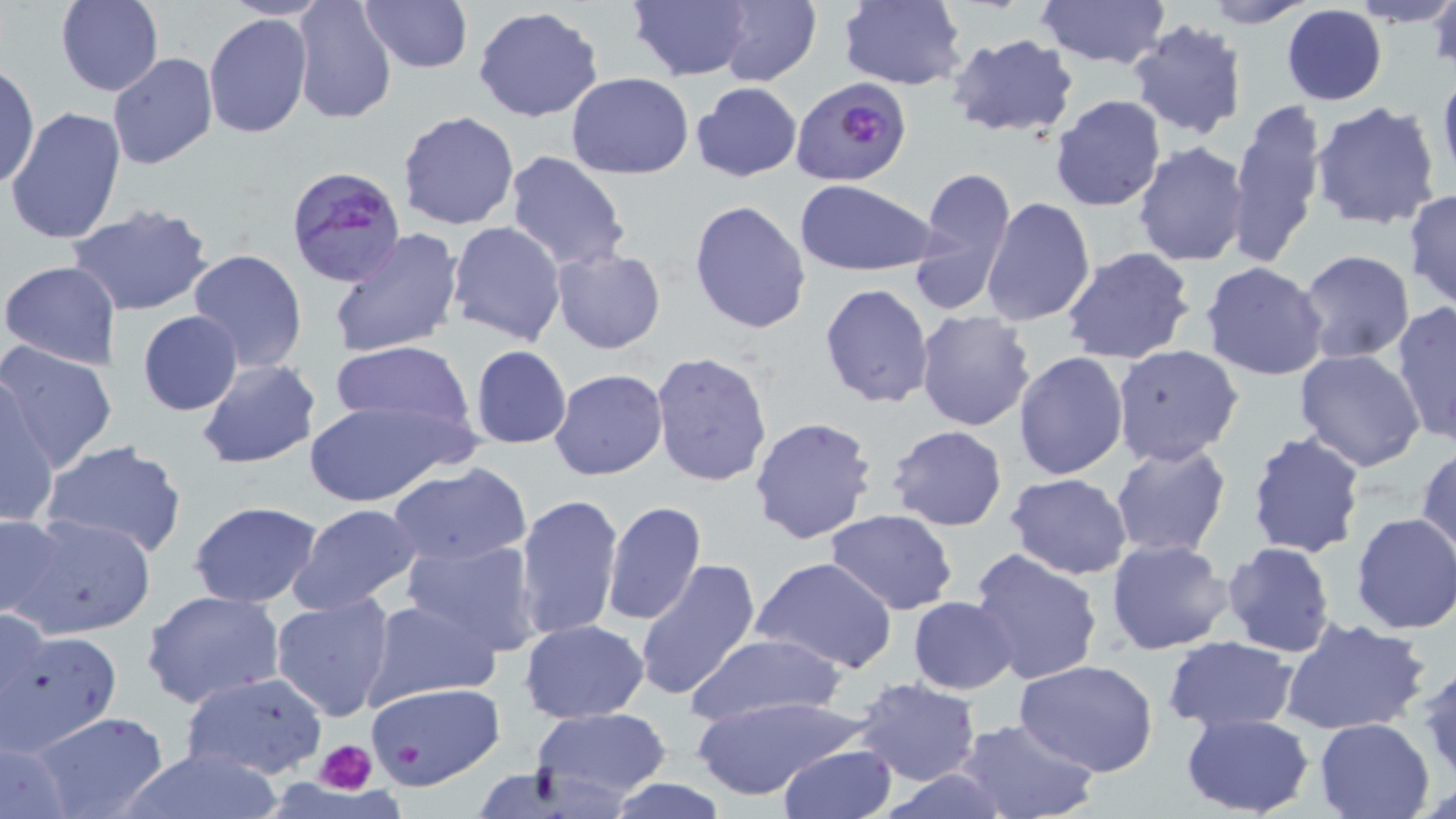 Approximate bounding boxes as (x1,y1)-(x2,y2) corner pairs in pixels. Plasmodium falciparum-infected red blood cell locations: (790,77)-(911,188), (284,163)-(408,288). Uninfected red blood cell locations: (220,0)-(328,21), (358,0)-(472,73), (627,0)-(754,81), (715,0)-(822,87), (837,0)-(966,90), (1034,0)-(1170,72), (1195,0)-(1315,28), (1349,0)-(1456,29), (1426,0)-(1456,73), (56,1)-(162,96), (291,1)-(397,125), (1280,5)-(1388,106), (472,6)-(605,123), (203,12)-(315,140), (1126,21)-(1248,140), (945,33)-(1080,140), (108,54)-(217,170), (1,61)-(38,191), (1084,67)-(1238,198), (1437,68)-(1456,191), (566,72)-(693,178), (691,81)-(802,182), (1049,95)-(1166,211), (1225,98)-(1328,268), (1310,100)-(1444,233), (5,109)-(127,247), (398,110)-(519,231), (1133,141)-(1250,266), (504,150)-(631,274), (910,166)-(1017,312), (795,179)-(937,276), (1404,189)-(1456,312), (981,197)-(1095,326), (689,199)-(811,334), (66,202)-(215,316), (447,221)-(566,347), (327,228)-(464,359), (1060,246)-(1197,364), (187,248)-(307,372), (552,249)-(666,354), (1298,250)-(1416,364), (1,260)-(124,369), (1200,262)-(1330,382), (819,283)-(935,409), (1390,301)-(1456,446), (915,308)-(1037,431), (137,310)-(245,415), (327,338)-(479,443), (0,340)-(119,473), (1110,343)-(1244,465), (469,346)-(572,448), (1294,348)-(1427,472), (649,350)-(774,488), (1012,351)-(1128,480), (194,358)-(323,470), (549,369)-(669,480), (0,379)-(59,530), (301,397)-(468,508), (748,414)-(878,544), (886,425)-(1008,531), (1247,431)-(1364,557), (40,439)-(189,559), (1110,441)-(1233,559), (1415,444)-(1456,568), (386,463)-(532,566), (1006,472)-(1132,579), (515,493)-(624,639), (189,500)-(322,605), (601,500)-(707,626), (288,501)-(425,614), (827,510)-(958,614), (0,511)-(69,621), (1351,512)-(1456,635), (8,513)-(157,640), (400,538)-(543,653), (1106,538)-(1235,656), (1222,542)-(1336,657), (968,548)-(1104,686), (634,558)-(763,703), (751,558)-(899,673), (141,589)-(287,711), (269,592)-(397,723), (908,595)-(1019,695), (361,598)-(500,710), (0,605)-(46,737), (1279,615)-(1432,736), (519,618)-(651,722), (2,625)-(122,753), (683,631)-(848,726), (1163,635)-(1297,731), (1418,658)-(1456,786), (1015,659)-(1160,778), (178,671)-(330,782), (852,677)-(982,785), (363,681)-(506,790), (689,695)-(866,802), (532,707)-(673,805), (27,710)-(170,819), (1180,714)-(1314,816), (954,716)-(1102,819), (1315,718)-(1435,819), (0,736)-(75,817), (776,744)-(899,819), (115,745)-(285,818), (878,767)-(1017,818), (604,778)-(732,817). Platelet locations: (317,738)-(380,796), (398,741)-(422,765). Slide-level diagnosis: Plasmodium falciparum. Image is 1456×819 pixels. 1000x magnification. Thin blood smear. Optical microscopy. Single field of view. May-Grünwald-Giemsa stain.